Assess the morphology of the red blood cells.
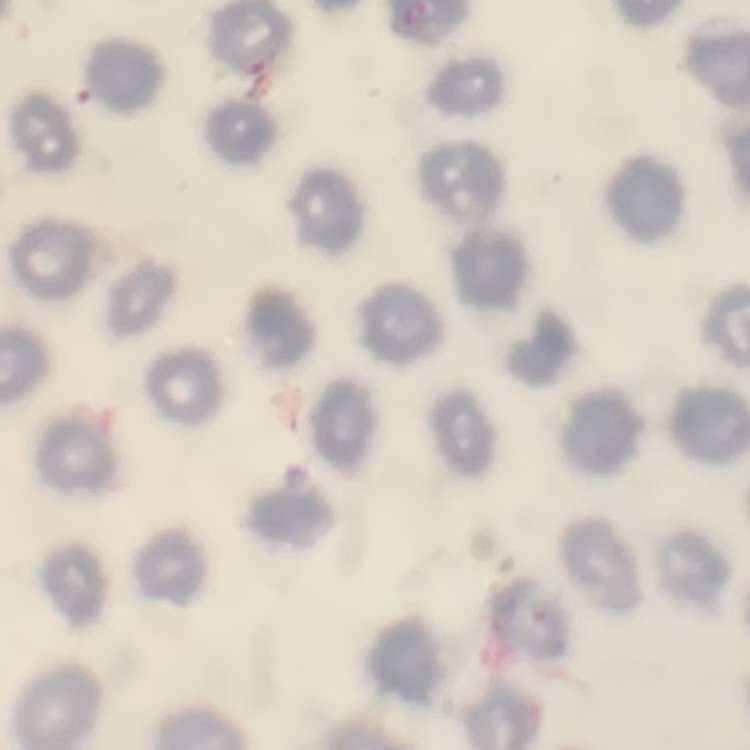
No rouleaux formation.

Summary:
  - Image type: square crop of a larger photomicrograph
  - Preparation: thin blood smear
  - Stain: Field's or Giemsa